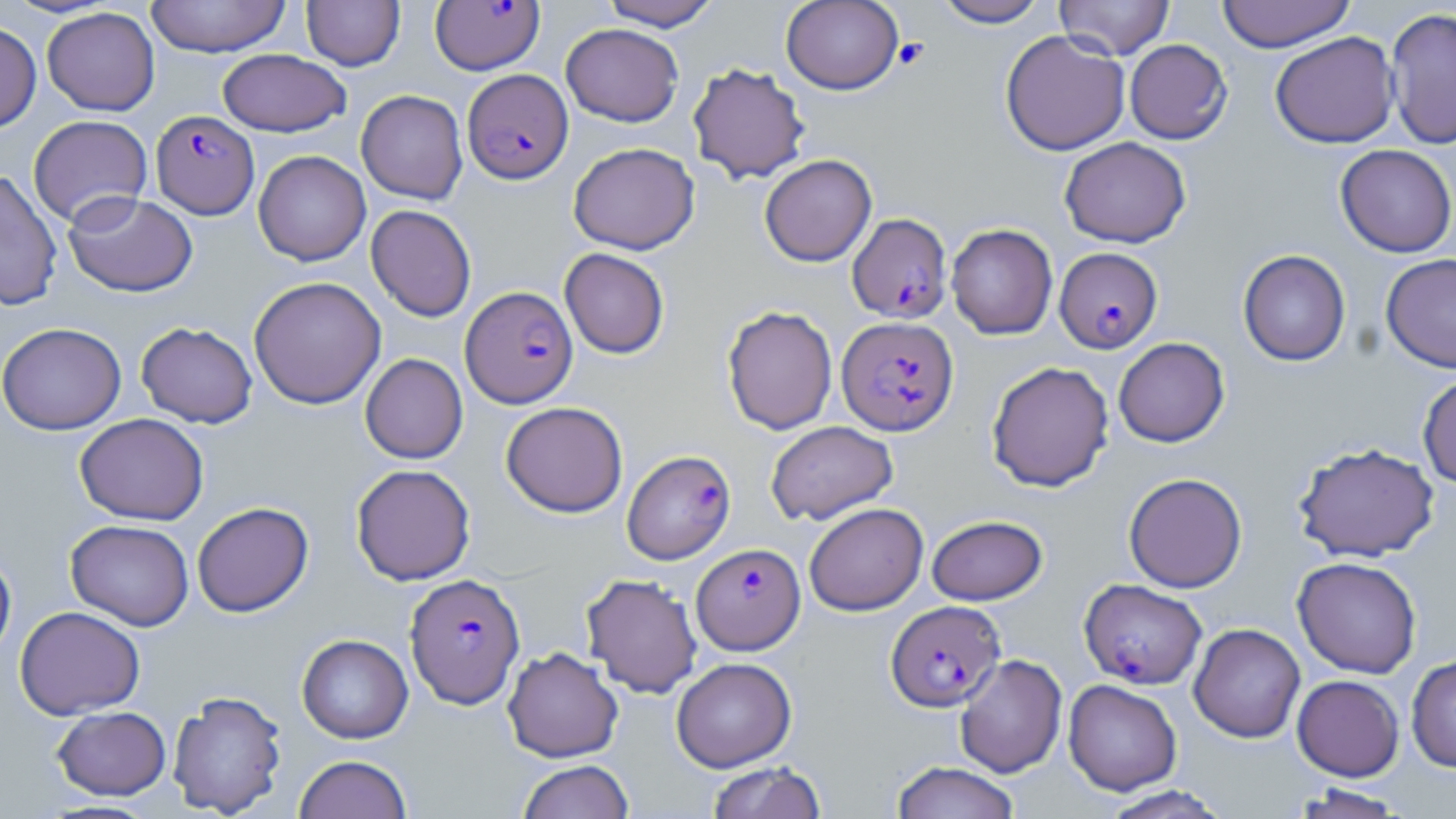

slide-level diagnosis = Plasmodium falciparum
image size = 1456×819 pixels
platelet locations = approximate bounding boxes as named x1/y1/x2/y2 corners in pixels: (x1=893, y1=37, x2=929, y2=70)
uninfected red blood cell locations = approximate bounding boxes as named x1/y1/x2/y2 corners in pixels: (x1=145, y1=0, x2=291, y2=57), (x1=301, y1=0, x2=405, y2=71), (x1=599, y1=0, x2=722, y2=30), (x1=780, y1=0, x2=904, y2=94), (x1=932, y1=0, x2=1049, y2=27), (x1=1054, y1=0, x2=1175, y2=60), (x1=1216, y1=0, x2=1356, y2=52), (x1=42, y1=7, x2=160, y2=116), (x1=1384, y1=7, x2=1456, y2=150), (x1=0, y1=21, x2=42, y2=133), (x1=561, y1=23, x2=684, y2=127), (x1=1000, y1=30, x2=1130, y2=156), (x1=1270, y1=31, x2=1399, y2=149), (x1=1124, y1=39, x2=1232, y2=144), (x1=217, y1=48, x2=352, y2=137), (x1=687, y1=62, x2=811, y2=184), (x1=356, y1=89, x2=468, y2=205), (x1=28, y1=115, x2=153, y2=228), (x1=1059, y1=137, x2=1191, y2=248), (x1=568, y1=142, x2=700, y2=254), (x1=1335, y1=145, x2=1455, y2=258), (x1=253, y1=150, x2=371, y2=266), (x1=759, y1=154, x2=877, y2=267), (x1=0, y1=170, x2=63, y2=311), (x1=63, y1=191, x2=198, y2=297), (x1=366, y1=204, x2=476, y2=322), (x1=946, y1=223, x2=1058, y2=340), (x1=560, y1=248, x2=670, y2=359), (x1=1238, y1=249, x2=1351, y2=367), (x1=1381, y1=253, x2=1456, y2=373), (x1=248, y1=276, x2=386, y2=409), (x1=722, y1=305, x2=838, y2=435), (x1=0, y1=322, x2=127, y2=435), (x1=136, y1=322, x2=257, y2=428), (x1=1113, y1=337, x2=1230, y2=447), (x1=360, y1=353, x2=468, y2=464), (x1=986, y1=360, x2=1114, y2=492), (x1=1417, y1=372, x2=1456, y2=488), (x1=501, y1=401, x2=628, y2=518), (x1=75, y1=413, x2=210, y2=525), (x1=765, y1=420, x2=899, y2=525), (x1=1293, y1=442, x2=1440, y2=563), (x1=351, y1=464, x2=475, y2=585), (x1=1123, y1=472, x2=1248, y2=593), (x1=192, y1=501, x2=314, y2=617), (x1=804, y1=502, x2=929, y2=616), (x1=927, y1=515, x2=1047, y2=605), (x1=65, y1=519, x2=194, y2=631), (x1=0, y1=547, x2=17, y2=668), (x1=1292, y1=556, x2=1422, y2=678), (x1=581, y1=573, x2=703, y2=698), (x1=14, y1=606, x2=146, y2=720), (x1=1188, y1=623, x2=1305, y2=743), (x1=297, y1=634, x2=413, y2=743), (x1=502, y1=647, x2=623, y2=762), (x1=953, y1=654, x2=1068, y2=778), (x1=1406, y1=655, x2=1456, y2=772), (x1=671, y1=657, x2=796, y2=772), (x1=1292, y1=674, x2=1404, y2=781), (x1=1063, y1=679, x2=1182, y2=796), (x1=167, y1=690, x2=288, y2=817), (x1=52, y1=706, x2=171, y2=800), (x1=294, y1=754, x2=413, y2=818), (x1=517, y1=759, x2=634, y2=819), (x1=707, y1=761, x2=827, y2=819), (x1=890, y1=761, x2=1021, y2=819), (x1=1290, y1=784, x2=1408, y2=818), (x1=1099, y1=786, x2=1234, y2=819)
stain = May-Grünwald-Giemsa
Plasmodium falciparum-infected red blood cell locations = approximate bounding boxes as named x1/y1/x2/y2 corners in pixels: (x1=430, y1=0, x2=545, y2=75), (x1=463, y1=68, x2=573, y2=183), (x1=151, y1=110, x2=259, y2=219), (x1=847, y1=213, x2=953, y2=323), (x1=1054, y1=247, x2=1162, y2=354), (x1=460, y1=286, x2=578, y2=408), (x1=836, y1=315, x2=959, y2=436), (x1=622, y1=449, x2=736, y2=564), (x1=691, y1=543, x2=805, y2=654), (x1=406, y1=573, x2=525, y2=709), (x1=1079, y1=578, x2=1207, y2=689), (x1=886, y1=601, x2=1005, y2=711)
modality = optical microscopy
field of view = one of a larger specimen
preparation = thin blood film
magnification = 1000x